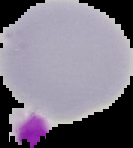 Segmented cell region on a black background. Result: no Plasmodium parasites detected. From a thin blood smear. Image is 133×148 pixels.